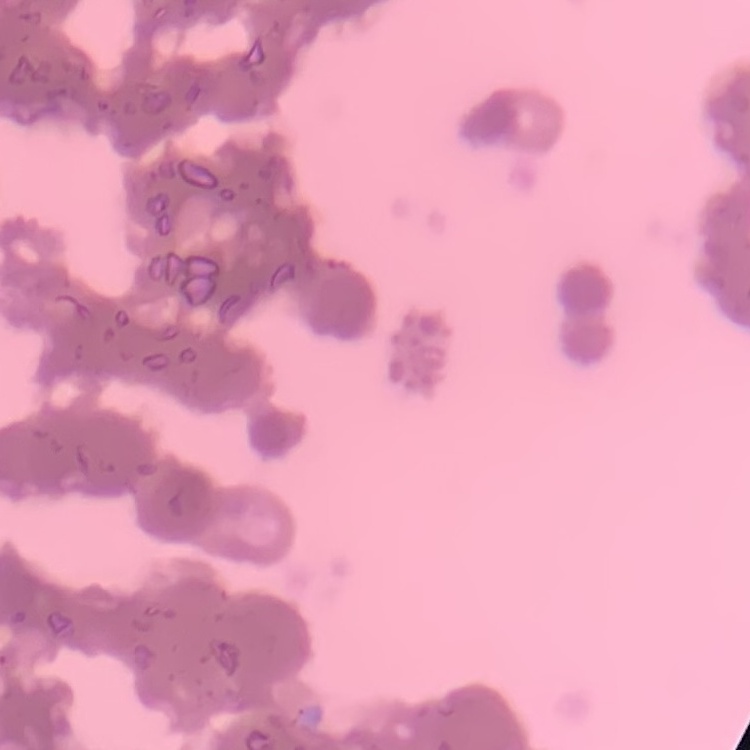

erythrocyte morphology = rouleaux formation
preparation = thin blood film
stain = Field's or Giemsa
image type = square crop of a larger photomicrograph